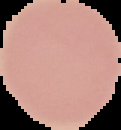
Image is 121×130 pixels. Segmented cell region on a black background. Malaria status: uninfected. From a thin blood film.